Assess this cell for malaria.
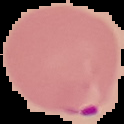

It is parasitized.

Image is 124×124 pixels. Cell region segmented out of the field of view; the surrounding area is masked to black. From a thin blood smear.